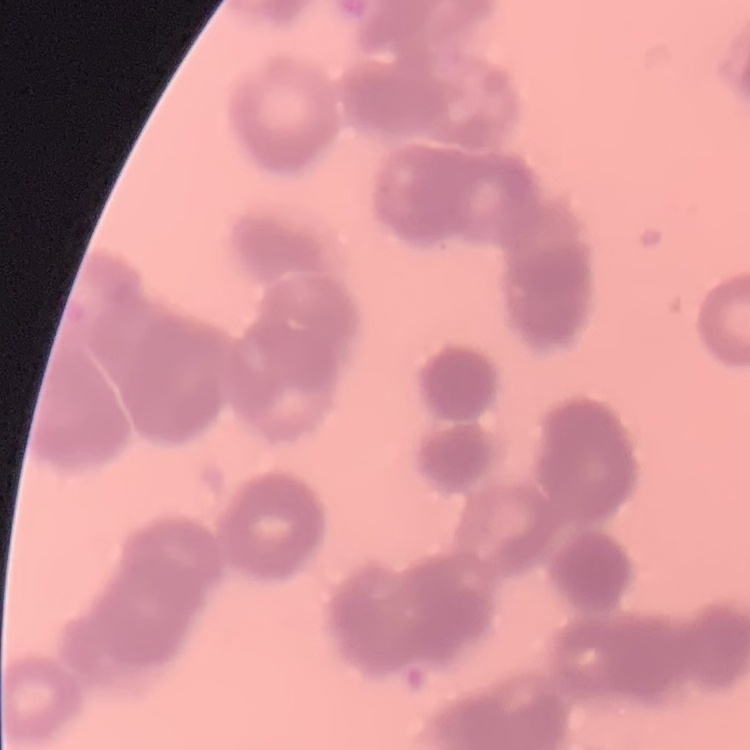
The erythrocytes show rouleaux formation. Thin peripheral smear. Field's or Giemsa stain. One tile cut from a larger photomicrograph.